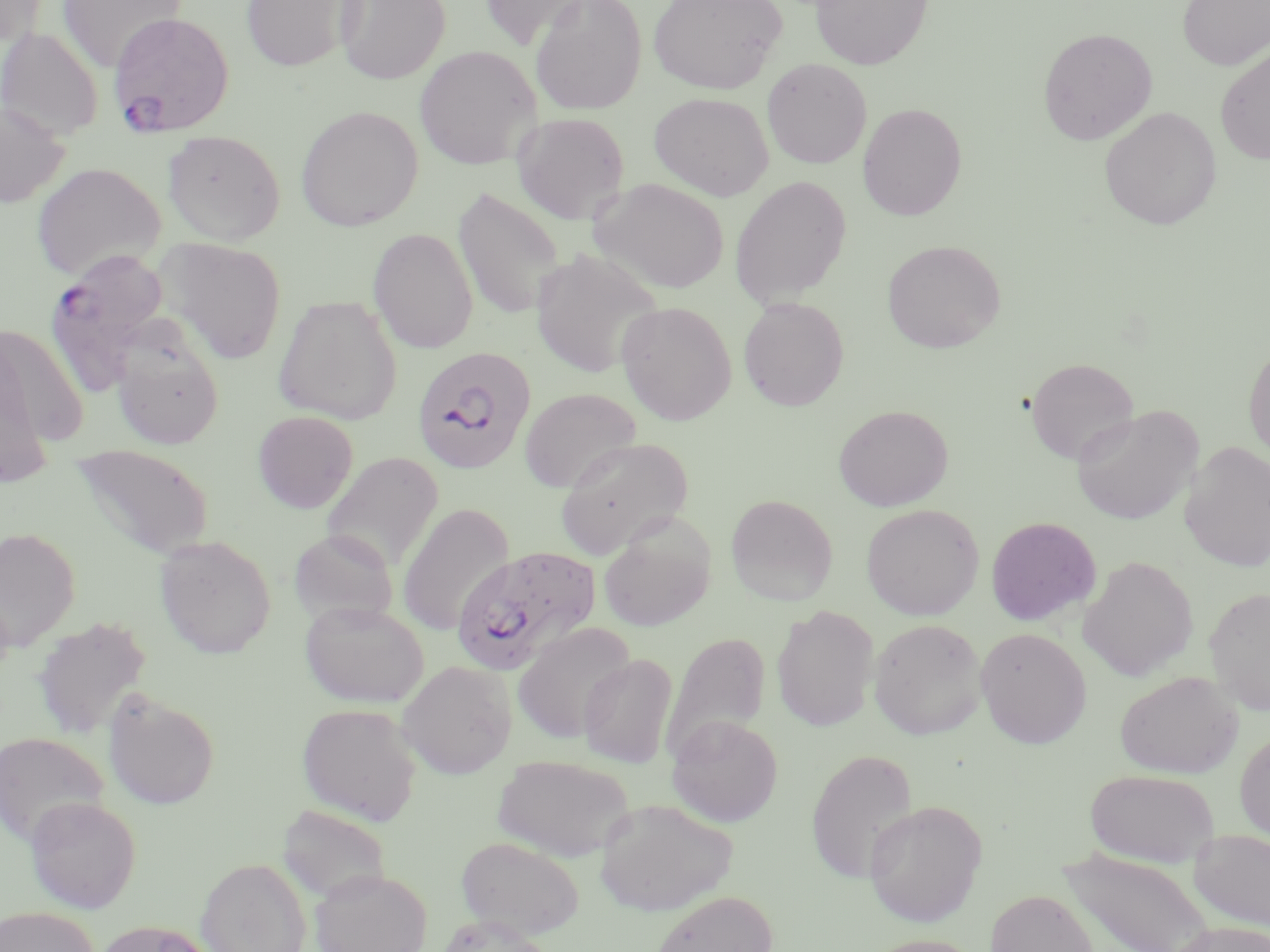

{
  "slide_level_diagnosis": "Plasmodium falciparum",
  "field_of_view": "single",
  "image_size": "1270×952 pixels",
  "magnification": "1000x",
  "plasmodium_falciparum_infected_red_blood_cell_locations": "approximate bounding boxes as [x1, y1, x2, y2] in pixels: [106, 12, 234, 138], [44, 248, 177, 391], [411, 346, 537, 474], [451, 545, 605, 677]",
  "modality": "light microscopy",
  "uninfected_red_blood_cell_locations": "approximate bounding boxes as [x1, y1, x2, y2] in pixels: [56, 0, 187, 72], [240, 0, 358, 71], [334, 0, 450, 84], [480, 0, 593, 51], [648, 0, 787, 94], [811, 0, 932, 70], [1178, 0, 1270, 70], [0, 1, 49, 51], [529, 1, 647, 116], [0, 27, 104, 141], [1037, 28, 1156, 145], [413, 45, 542, 170], [1215, 46, 1270, 164], [762, 58, 872, 169], [649, 92, 775, 200], [0, 101, 69, 209], [858, 103, 967, 221], [295, 105, 424, 232], [1099, 106, 1221, 230], [512, 112, 631, 224], [162, 129, 285, 245], [31, 161, 165, 280], [729, 175, 852, 308], [590, 177, 730, 294], [452, 187, 567, 320], [368, 227, 479, 353], [160, 238, 288, 363], [882, 239, 1006, 353], [529, 247, 663, 378], [273, 294, 403, 425], [738, 296, 849, 411], [616, 301, 737, 425], [0, 324, 89, 446], [112, 331, 224, 450], [0, 335, 50, 478], [1244, 341, 1270, 464], [1026, 357, 1139, 465], [520, 387, 641, 493], [834, 405, 953, 511], [1071, 405, 1203, 526], [252, 410, 358, 514], [556, 437, 694, 558], [1179, 441, 1270, 573], [70, 443, 213, 560], [322, 451, 444, 571], [725, 493, 838, 606], [397, 502, 514, 635], [861, 504, 983, 620], [985, 516, 1102, 626], [598, 519, 715, 631], [0, 527, 81, 651], [287, 529, 399, 626], [155, 535, 277, 659], [1078, 555, 1199, 681], [1203, 586, 1270, 713], [299, 600, 429, 709], [771, 604, 879, 733], [33, 616, 151, 740], [869, 618, 988, 740], [512, 622, 636, 742], [974, 627, 1091, 748], [662, 631, 771, 758], [578, 654, 679, 769], [398, 659, 517, 778], [1115, 670, 1243, 778], [102, 690, 220, 809], [297, 702, 423, 825], [667, 714, 783, 827], [1235, 727, 1270, 845], [0, 732, 109, 846], [806, 749, 919, 884], [492, 754, 636, 861], [1085, 769, 1218, 867], [25, 796, 141, 913], [594, 798, 737, 916], [863, 799, 988, 927], [276, 803, 392, 905], [1189, 828, 1270, 931], [456, 835, 585, 939], [1059, 847, 1212, 952], [196, 858, 311, 952], [310, 868, 432, 952], [986, 889, 1099, 952], [649, 890, 778, 952], [0, 906, 99, 952], [436, 914, 550, 952], [93, 919, 216, 952], [1165, 920, 1270, 952], [859, 933, 985, 952]",
  "preparation": "thin blood film",
  "stain": "May-Grünwald-Giemsa"
}